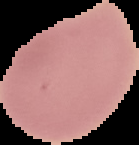
Summary:
  - Image size: 139×145 pixels
  - Image type: segmented cell region on a black background
  - Malaria status: uninfected
  - Preparation: thin blood film